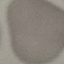

Summary:
  - Result: negative for malaria parasites
  - Image type: cell patch, automatically extracted from a larger field of view and resized to 64 × 64 pixels
  - Capture: smartphone camera at the microscope eyepiece
  - Preparation: thin smear
  - Stain: Giemsa